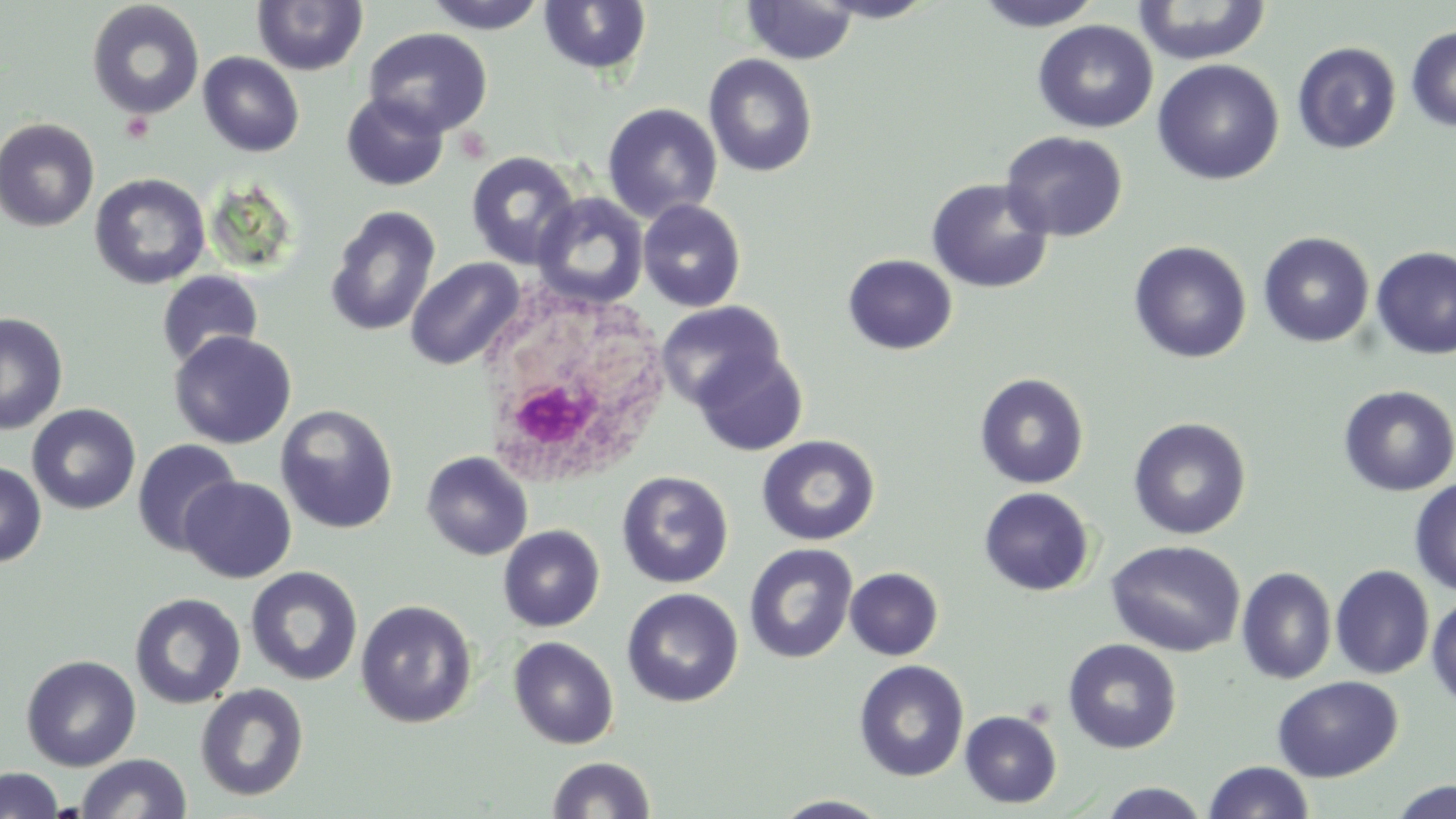

Summary:
  - Coordinate format: approximate bounding boxes as (x1,y1)-(x2,y2) corner pairs in pixels
  - Uninfected red blood cell locations: (423,0)-(549,34), (813,0)-(942,23), (973,0)-(1105,31), (86,1)-(204,120), (252,1)-(368,75), (539,1)-(653,77), (742,1)-(858,65), (1132,1)-(1273,65), (1033,19)-(1158,134), (1405,25)-(1456,133), (363,27)-(493,138), (1292,42)-(1401,154), (198,52)-(304,157), (703,53)-(818,178), (1152,59)-(1284,185), (341,91)-(449,191), (602,102)-(723,223), (0,117)-(100,231), (1000,130)-(1129,242), (465,151)-(580,269), (89,173)-(211,290), (926,177)-(1054,294), (533,193)-(649,308), (638,199)-(746,312), (325,205)-(441,337), (1257,232)-(1375,347), (1128,241)-(1252,364), (1371,246)-(1456,359), (843,254)-(958,355), (405,258)-(525,370), (156,270)-(264,369), (657,301)-(786,412), (0,312)-(68,435), (169,331)-(297,449), (692,348)-(808,456), (974,372)-(1089,489), (1338,385)-(1456,497), (27,403)-(141,515), (276,404)-(398,534), (1128,417)-(1251,540), (756,434)-(880,546), (132,438)-(242,556), (421,451)-(533,561), (0,461)-(47,567), (617,470)-(734,589), (180,476)-(296,583), (1409,477)-(1456,596), (978,487)-(1095,596), (498,525)-(605,632), (1106,540)-(1247,657), (744,543)-(857,664), (1331,565)-(1435,680), (245,566)-(363,686), (845,567)-(943,660), (1236,567)-(1337,684), (622,588)-(744,707), (1426,592)-(1456,709), (130,593)-(246,709), (356,599)-(477,728), (508,636)-(619,749), (1063,639)-(1183,754), (21,654)-(141,771), (854,660)-(970,781), (1271,675)-(1403,782), (195,683)-(309,802), (960,710)-(1062,808), (77,753)-(190,819), (548,756)-(655,818), (1202,761)-(1315,819), (0,767)-(63,818), (1388,780)-(1456,819), (1097,783)-(1211,818), (771,795)-(893,818)
  - White blood cell locations: (478,289)-(672,494)
  - Slide-level diagnosis: no evidence of blood parasites
  - Stain: May-Grünwald-Giemsa
  - Preparation: thin blood smear
  - Modality: light microscopy
  - Field of view: single
  - Image size: 1456×819 pixels
  - Magnification: 1000x